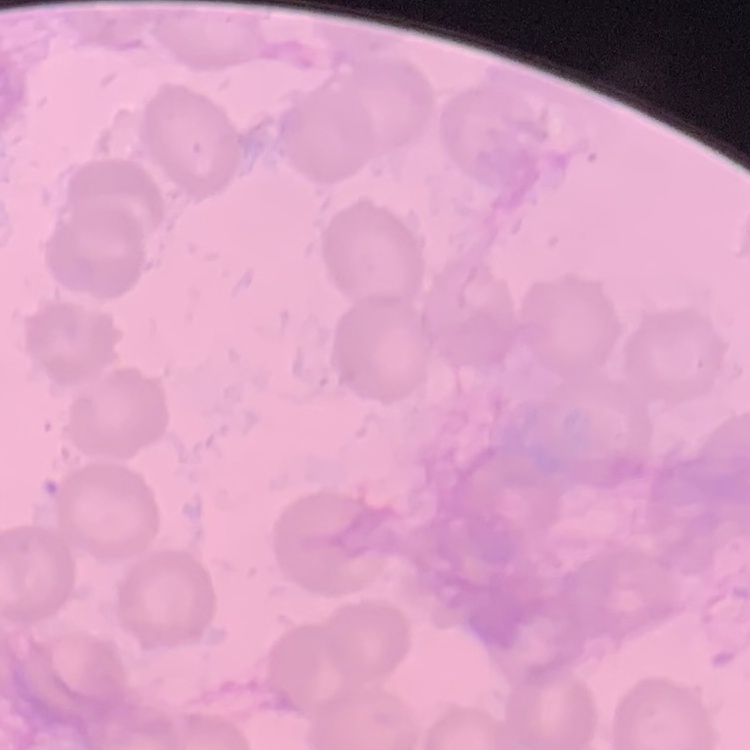
{
  "red_blood_cell_morphology": "no rouleaux formation",
  "image_type": "square crop of a larger photomicrograph",
  "preparation": "thin blood smear",
  "stain": "Field's or Giemsa"
}